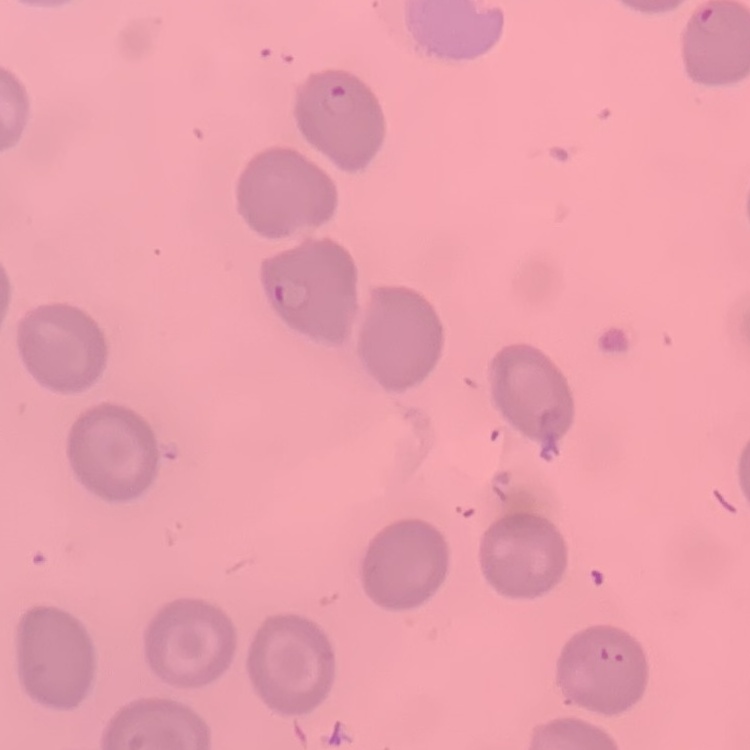
Summary:
  - Erythrocyte morphology: no rouleaux formation
  - Image type: one tile cut from a larger photomicrograph
  - Stain: Field's or Giemsa
  - Preparation: thin blood film